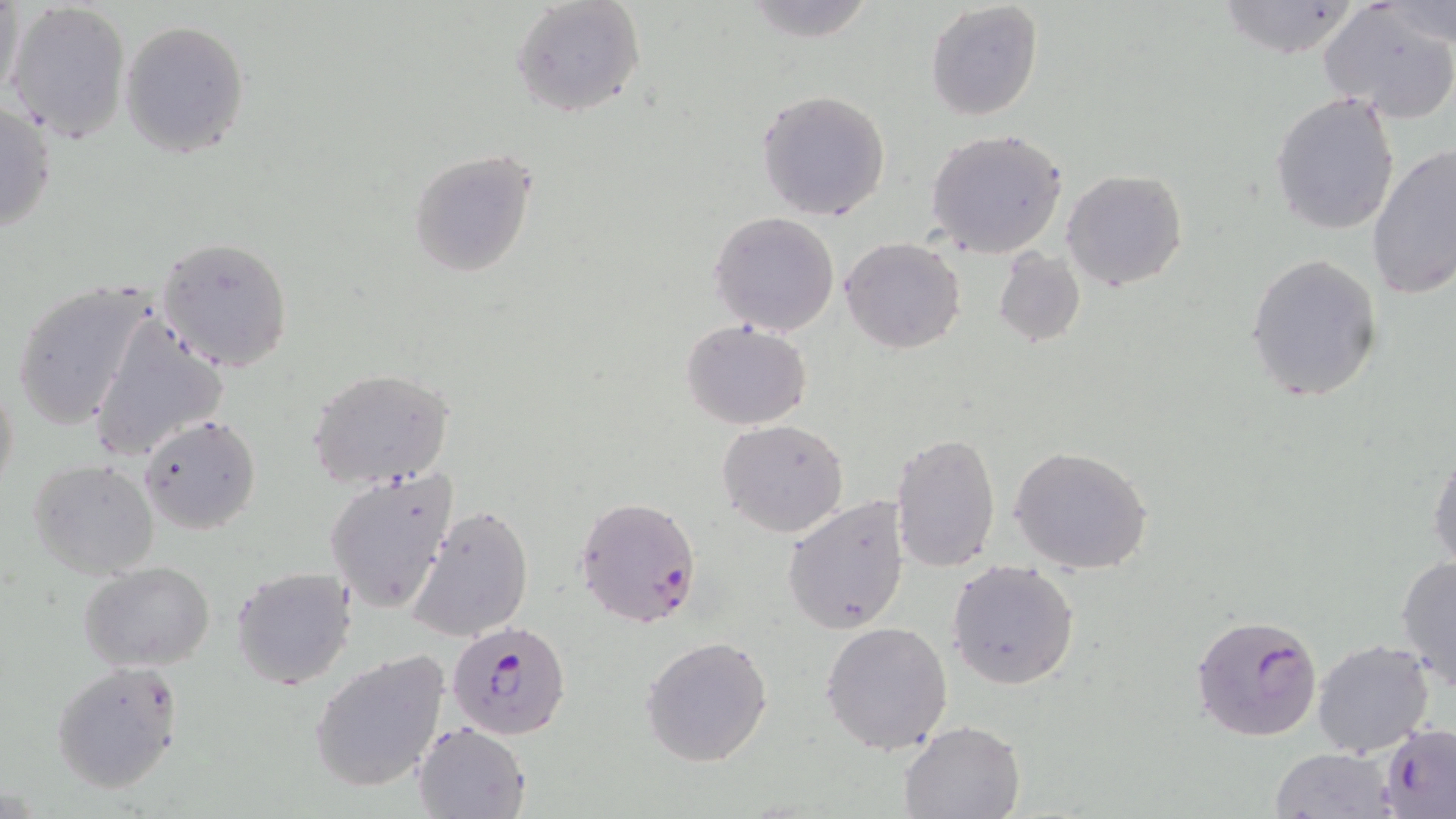

Approximate bounding boxes as (x1, y1, x2, y2) in pixels. Plasmodium falciparum-infected red blood cell locations: (574, 494, 703, 629), (1192, 615, 1322, 742), (446, 618, 574, 741), (1380, 724, 1456, 816). Uninfected red blood cell locations: (1, 0, 27, 106), (509, 0, 646, 118), (1217, 0, 1359, 56), (5, 1, 131, 145), (742, 1, 880, 44), (924, 1, 1043, 120), (1319, 2, 1456, 123), (1383, 2, 1456, 50), (120, 19, 251, 160), (756, 89, 891, 222), (1270, 90, 1402, 236), (0, 97, 57, 239), (925, 128, 1067, 257), (1366, 143, 1456, 301), (407, 148, 538, 279), (1061, 170, 1188, 292), (708, 212, 840, 336), (157, 236, 293, 372), (841, 237, 965, 354), (994, 249, 1086, 348), (1246, 254, 1385, 403), (9, 277, 155, 433), (85, 309, 230, 464), (681, 319, 812, 429), (305, 367, 456, 489), (0, 368, 20, 505), (138, 413, 262, 535), (717, 419, 850, 538), (890, 430, 1002, 574), (1010, 446, 1153, 575), (1429, 452, 1456, 574), (28, 458, 159, 580), (324, 470, 457, 613), (781, 495, 909, 634), (405, 503, 537, 643), (1396, 555, 1456, 691), (945, 558, 1080, 689), (79, 563, 216, 673), (229, 564, 358, 690), (821, 622, 952, 754), (640, 635, 773, 766), (1311, 637, 1435, 757), (309, 648, 450, 793), (51, 661, 184, 792), (898, 720, 1025, 818), (412, 721, 530, 819), (1268, 748, 1399, 819). Slide-level diagnosis: Plasmodium falciparum. Light microscopy. 1000x magnification. Thin blood film. One field of a larger specimen. May-Grünwald-Giemsa-stained preparation. Image is 1456×819 pixels.